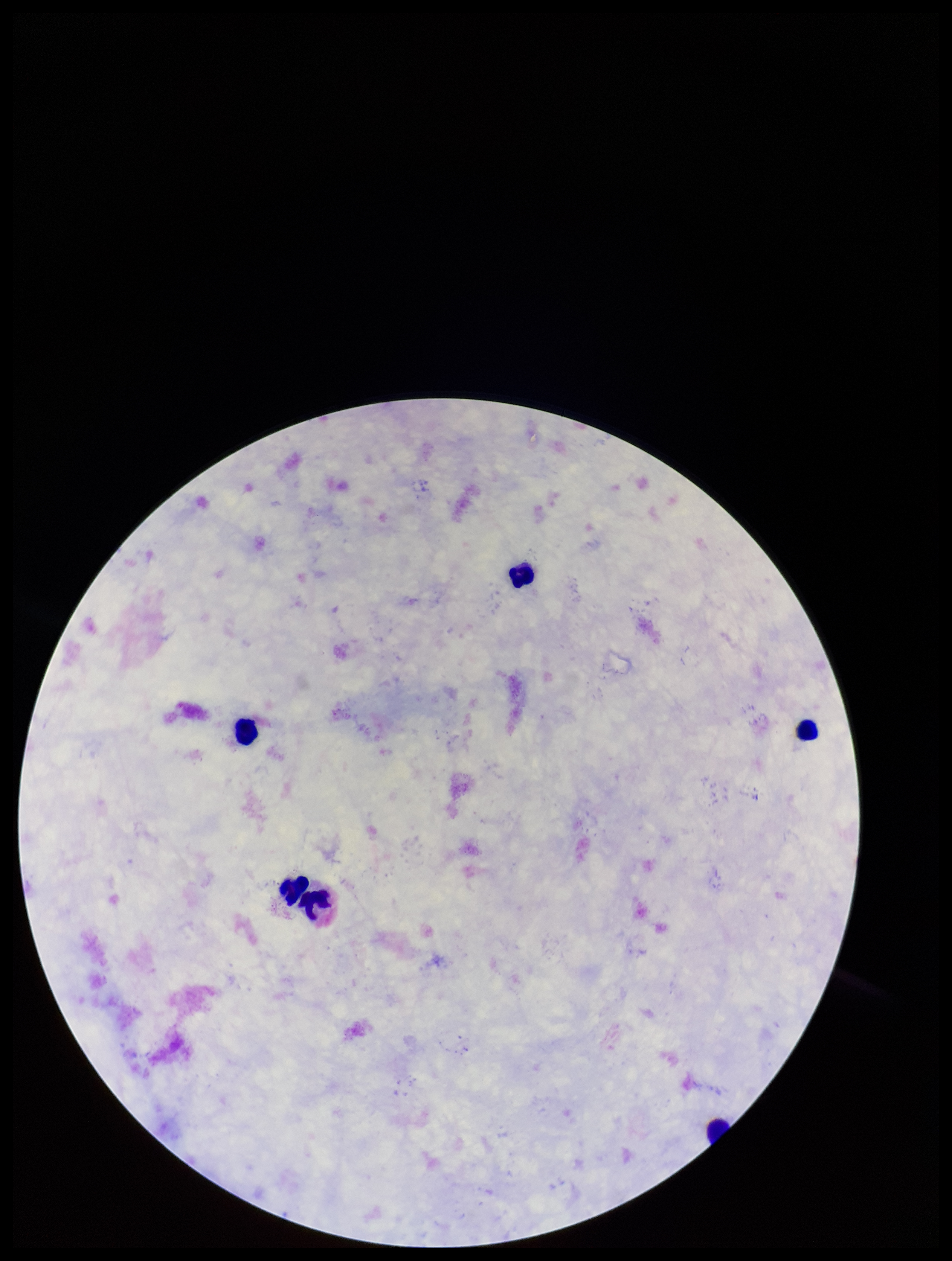

Parasite count: 0. Plasmodium parasites: none detected. Patient malaria status: negative. Image is 952×1261 pixels. Giemsa stain. Leukocyte count: 6. Single field of view. Preparation: thick. Photographed through the microscope eyepiece with a smartphone camera.